Classify this cell by malaria status.
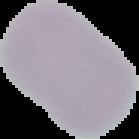

It is uninfected.

From a thin blood film. Image is 139×139 pixels. Cell region segmented out of the field of view; the surrounding area is masked to black.